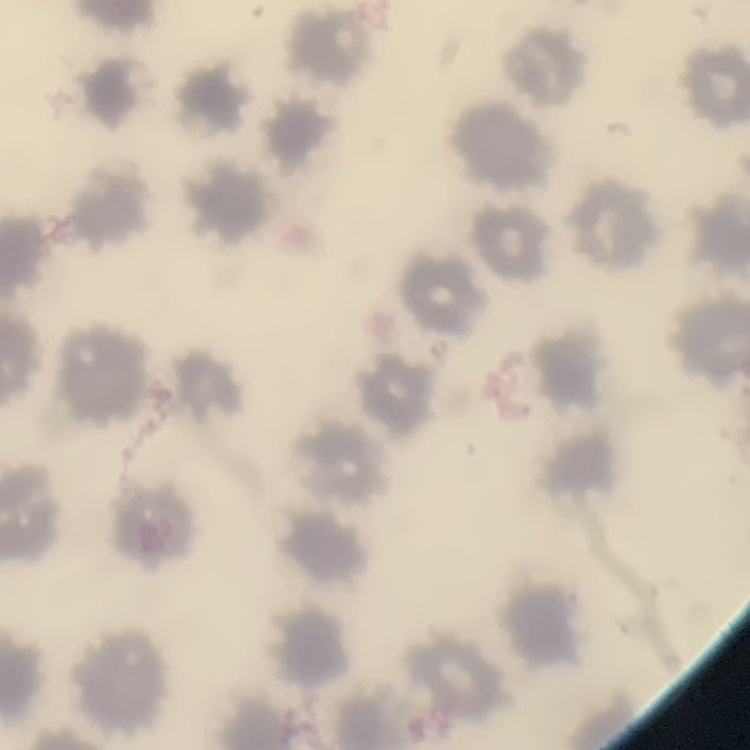

erythrocyte morphology = no rouleaux formation
stain = Field's or Giemsa
preparation = thin blood film
image type = square crop of a larger photomicrograph